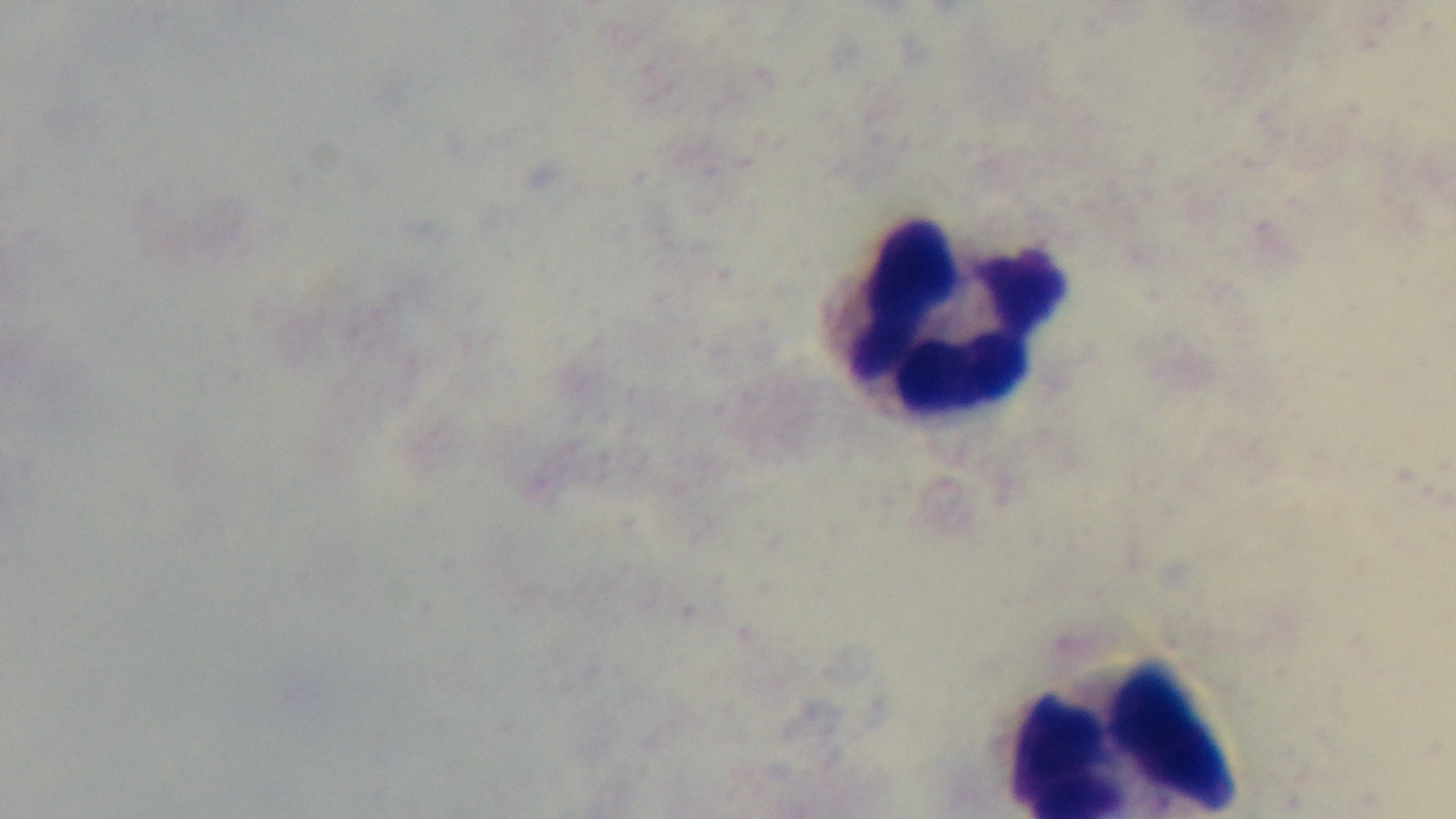 One field from the slide. Photomicrograph. Mounted 4K digital camera. Malaria status: negative. Preparation: thick blood film. Oil-immersion objective, 100x. Giemsa stain.